Outline each blood parasite and name the species.
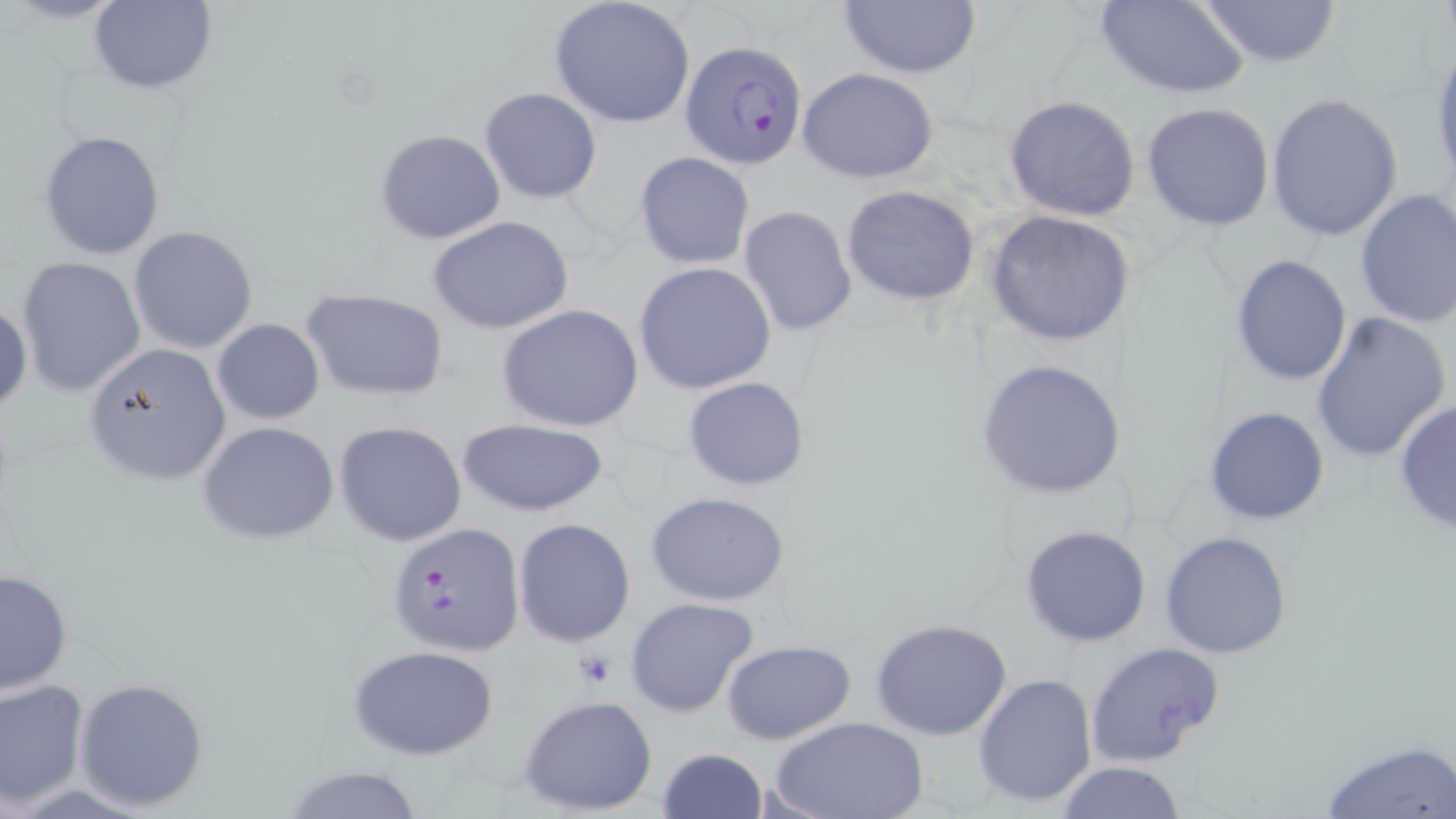
Approximate bounding boxes as (x1,y1)-(x2,y2) corner pairs in pixels.
Plasmodium falciparum-infected red blood cells: (682,40)-(811,169), (386,522)-(526,656).
No Plasmodium ovale, Plasmodium malariae, Plasmodium vivax, Babesia divergens, or Trypanosoma brucei observed.

Summary:
  - Uninfected red blood cell locations: (86,0)-(217,94), (835,0)-(984,78), (1097,0)-(1251,98), (1192,0)-(1345,67), (549,1)-(697,128), (1429,41)-(1456,192), (796,66)-(941,184), (479,87)-(602,204), (1265,92)-(1403,241), (1003,94)-(1141,222), (1141,102)-(1275,231), (374,128)-(505,244), (40,129)-(165,260), (634,151)-(755,270), (842,185)-(980,306), (1353,189)-(1456,330), (738,206)-(857,336), (985,209)-(1138,346), (426,215)-(573,335), (129,226)-(258,354), (1229,254)-(1353,387), (16,256)-(146,396), (634,261)-(777,395), (301,287)-(448,402), (0,300)-(30,417), (495,304)-(643,431), (1310,311)-(1452,463), (211,319)-(325,424), (82,343)-(233,486), (975,358)-(1127,500), (683,377)-(811,491), (1393,399)-(1455,534), (1204,406)-(1331,526), (335,419)-(468,546), (456,419)-(610,517), (198,420)-(339,545), (644,492)-(790,606), (512,517)-(636,646), (1018,523)-(1152,647), (1158,530)-(1292,660), (0,569)-(71,697), (624,597)-(763,720), (869,617)-(1013,741), (722,639)-(856,744), (1084,642)-(1226,768), (348,644)-(501,760), (973,673)-(1097,808), (0,677)-(90,806), (74,677)-(210,812), (518,694)-(659,816), (771,714)-(926,819), (1317,739)-(1456,818), (656,747)-(767,819), (1054,761)-(1187,818), (277,765)-(426,819)
  - Platelet locations: (572,648)-(621,690)
  - Slide-level diagnosis: Plasmodium falciparum
  - Magnification: 1000x
  - Stain: May-Grünwald-Giemsa
  - Field of view: one of a larger specimen
  - Preparation: thin blood film
  - Image size: 1456×819 pixels
  - Modality: light microscopy